Report the malaria status of this cell.
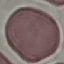
It is uninfected.

image type = cell patch, automatically extracted from a larger field of view and resized to 64 × 64 pixels
stain = Giemsa
capture = smartphone through the microscope eyepiece
preparation = thin blood film